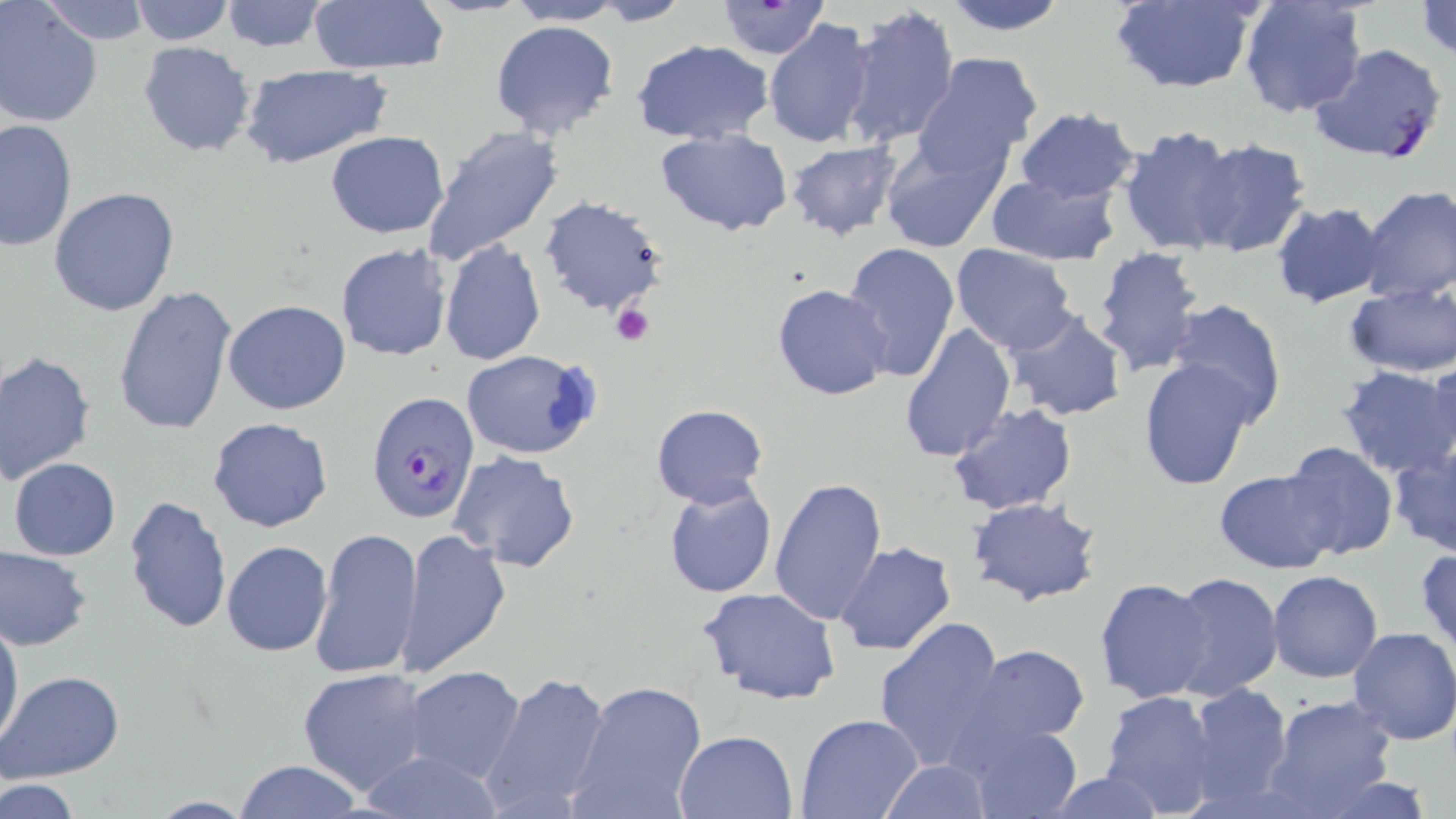
Summary:
  - Coordinate format: approximate bounding boxes as (x1, y1, x2, y2) in pixels
  - Uninfected red blood cell locations: (41, 0, 149, 46), (130, 0, 234, 46), (217, 0, 331, 53), (939, 0, 1069, 36), (1108, 0, 1262, 93), (1238, 0, 1369, 121), (505, 1, 624, 25), (590, 1, 694, 25), (713, 1, 831, 59), (1414, 1, 1456, 57), (307, 2, 449, 75), (0, 3, 104, 129), (841, 5, 961, 150), (489, 17, 620, 140), (764, 17, 876, 149), (631, 40, 774, 147), (137, 41, 257, 158), (913, 54, 1044, 177), (241, 66, 392, 167), (1012, 105, 1141, 206), (0, 118, 77, 253), (420, 124, 565, 266), (1116, 125, 1241, 254), (654, 128, 793, 236), (325, 131, 450, 238), (879, 135, 1008, 253), (1187, 137, 1312, 257), (784, 141, 901, 240), (984, 174, 1120, 266), (1359, 184, 1456, 304), (48, 187, 180, 317), (539, 197, 671, 318), (1271, 201, 1389, 310), (440, 237, 546, 365), (842, 242, 960, 380), (335, 243, 454, 362), (951, 243, 1076, 355), (1091, 246, 1207, 378), (1343, 282, 1455, 378), (771, 284, 895, 401), (112, 285, 239, 438), (1166, 299, 1287, 425), (223, 300, 351, 415), (1003, 308, 1127, 422), (898, 322, 1015, 461), (461, 349, 601, 460), (1, 350, 97, 483), (1139, 356, 1259, 489), (1422, 359, 1456, 471), (1334, 366, 1456, 479), (948, 402, 1077, 515), (651, 403, 769, 509), (207, 417, 334, 534), (1279, 440, 1399, 560), (1386, 445, 1456, 559), (450, 451, 581, 573), (8, 457, 121, 561), (1213, 467, 1338, 574), (768, 475, 888, 626), (662, 479, 779, 600), (122, 494, 233, 634), (967, 497, 1103, 607), (309, 524, 420, 679), (396, 528, 512, 679), (221, 539, 333, 656), (833, 541, 957, 657), (1, 545, 94, 650), (1415, 547, 1456, 661), (1266, 570, 1382, 682), (1165, 572, 1283, 698), (1095, 577, 1214, 705), (698, 586, 842, 705), (0, 614, 24, 752), (875, 616, 1008, 772), (1347, 626, 1456, 745), (967, 645, 1090, 747), (405, 665, 526, 781), (297, 667, 432, 797), (480, 669, 613, 817), (1, 670, 124, 781), (569, 679, 708, 819), (1187, 681, 1294, 809), (1099, 689, 1225, 819), (1262, 694, 1399, 817), (795, 714, 924, 818), (953, 716, 1084, 818), (674, 728, 798, 818), (357, 748, 503, 819), (232, 760, 366, 818), (878, 760, 993, 817), (1042, 770, 1167, 819), (1309, 775, 1444, 819), (2, 776, 81, 819), (144, 796, 255, 818)
  - Plasmodium falciparum-infected red blood cell locations: (1308, 42, 1448, 166), (366, 394, 479, 528)
  - Platelet locations: (612, 303, 655, 345)
  - Slide-level diagnosis: Plasmodium falciparum
  - Field of view: one of a larger specimen
  - Preparation: thin blood film
  - Magnification: 1000x
  - Modality: optical microscopy
  - Image size: 1456×819 pixels
  - Stain: May-Grünwald-Giemsa